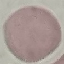

Result: negative for malaria parasites. Acquired by smartphone through the microscope eyepiece. Giemsa-stained preparation. Cell patch, automatically extracted from a larger field of view and resized to 64 × 64 pixels. Thin smear of blood.